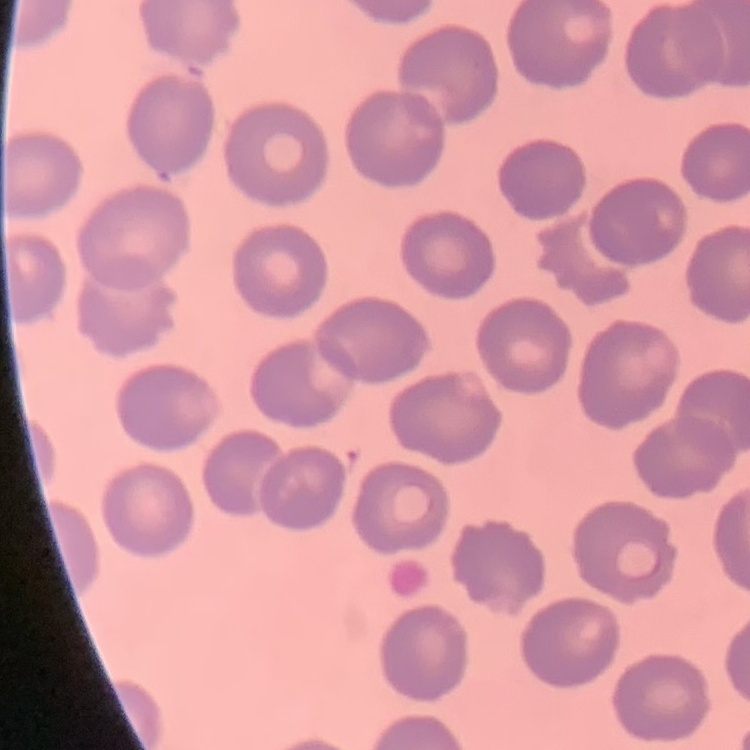
The erythrocytes exhibit no rouleaux formation. Thin peripheral smear. Square crop of a larger photomicrograph. Stained with either Field's or Giemsa.